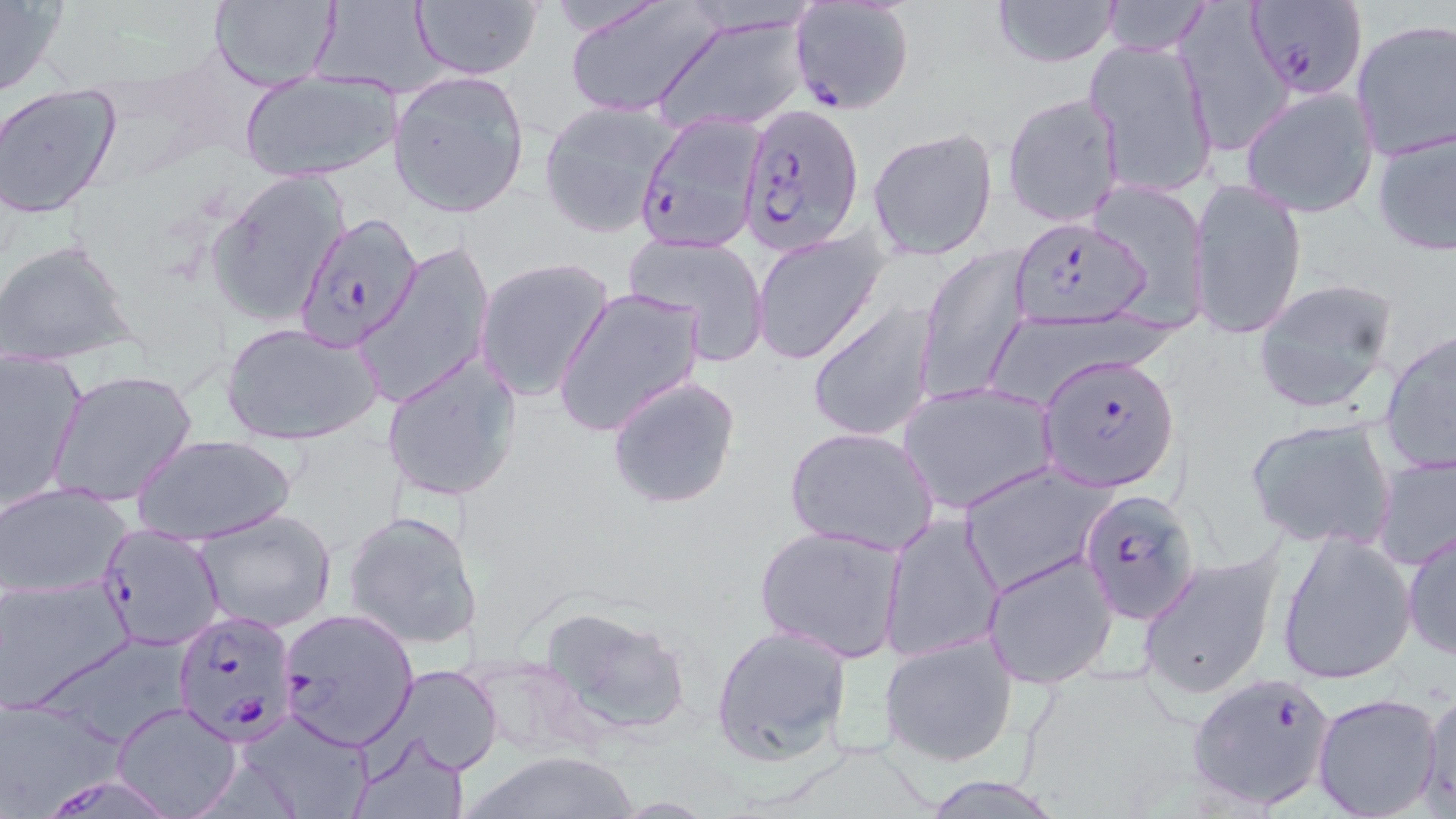
slide-level diagnosis = Plasmodium falciparum
modality = optical microscopy
stain = May-Grünwald-Giemsa
magnification = 1000x
Plasmodium falciparum-infected red blood cell locations (subset) = approximate bounding boxes as [x1, y1, x2, y2] in pixels: [1245, 0, 1365, 99], [787, 2, 915, 115], [737, 103, 864, 256], [291, 213, 422, 354], [1006, 218, 1151, 331], [1036, 352, 1178, 491], [1076, 486, 1202, 622], [98, 525, 225, 650], [277, 607, 419, 751], [172, 609, 298, 743], [1187, 671, 1339, 809], [50, 770, 166, 816]
image size = 1456×819 pixels
field of view = one of a larger specimen
preparation = thin blood film
uninfected red blood cell locations (subset) = approximate bounding boxes as [x1, y1, x2, y2] in pixels: [208, 0, 340, 89], [410, 0, 544, 81], [989, 0, 1122, 68], [1175, 0, 1291, 156], [564, 1, 724, 119], [1097, 1, 1214, 56], [0, 2, 65, 98], [311, 3, 442, 95], [653, 13, 814, 136], [1351, 21, 1456, 162], [1085, 36, 1219, 202], [240, 70, 399, 183], [387, 70, 531, 218], [0, 85, 122, 218], [1241, 86, 1378, 215], [1002, 91, 1124, 228], [539, 101, 678, 238], [1370, 120, 1456, 261], [868, 126, 999, 260], [207, 169, 348, 327], [1188, 175, 1307, 343], [1088, 180, 1210, 330], [750, 228, 888, 366], [624, 231, 772, 364], [0, 239, 139, 367], [360, 243, 492, 410], [917, 246, 1031, 404], [474, 258, 615, 402], [1248, 278, 1400, 415], [552, 287, 705, 439], [806, 301, 936, 442], [221, 320, 382, 447], [1379, 330, 1456, 476], [1, 348, 86, 511], [380, 353, 523, 503], [49, 370, 199, 508], [605, 374, 742, 511], [898, 380, 1057, 515], [1244, 415, 1397, 552], [784, 426, 940, 557], [132, 432, 296, 545], [1372, 450, 1456, 572], [958, 463, 1113, 595], [0, 482, 133, 600], [193, 509, 338, 633], [343, 509, 484, 651], [880, 512, 1003, 661], [752, 525, 905, 664], [1275, 527, 1418, 688], [1403, 528, 1456, 663], [1136, 547, 1285, 703], [982, 549, 1119, 688], [0, 576, 133, 712], [534, 603, 694, 739], [710, 623, 854, 765], [878, 630, 1018, 768], [460, 655, 601, 762], [380, 665, 504, 775], [1419, 686, 1456, 811], [1312, 693, 1443, 819], [0, 700, 114, 817], [113, 703, 242, 817], [235, 708, 377, 818], [350, 730, 471, 819], [456, 749, 645, 819], [921, 777, 1063, 816]